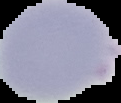
Summary:
  - Image size: 121×103 pixels
  - Image type: segmented cell region with the area outside set to black
  - Result: negative for Plasmodium parasites
  - Preparation: thin blood smear